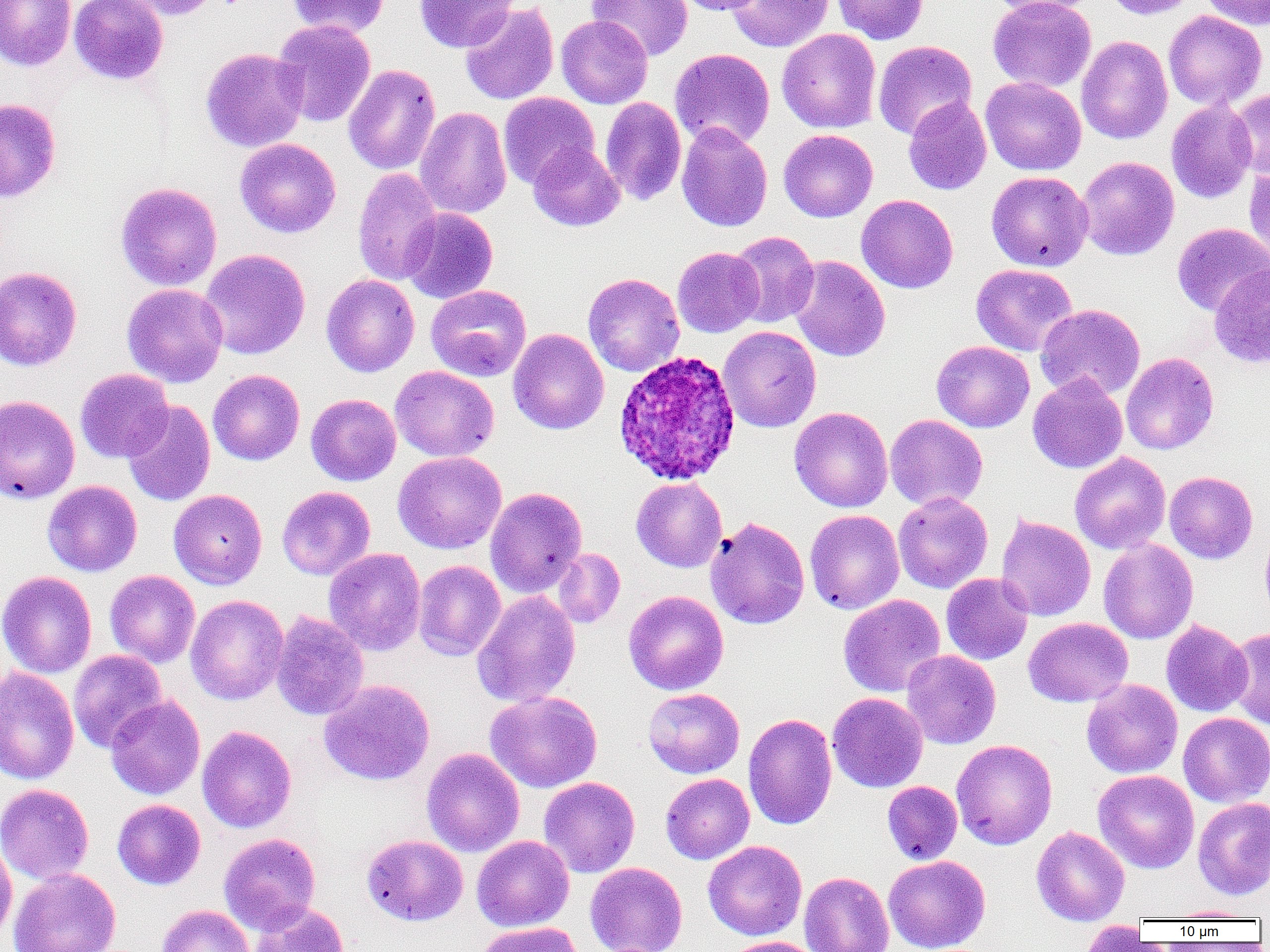

Approximate bounding boxes as named x1/y1/x2/y2 corners in pixels. Plasmodium ovale-infected red blood cell locations: (x1=613, y1=349, x2=741, y2=486). Uninfected red blood cell locations: (x1=0, y1=0, x2=76, y2=71), (x1=69, y1=0, x2=168, y2=85), (x1=116, y1=0, x2=223, y2=20), (x1=285, y1=0, x2=392, y2=38), (x1=415, y1=0, x2=518, y2=52), (x1=586, y1=0, x2=693, y2=61), (x1=674, y1=0, x2=765, y2=15), (x1=726, y1=0, x2=834, y2=52), (x1=832, y1=0, x2=929, y2=44), (x1=985, y1=0, x2=1098, y2=17), (x1=987, y1=0, x2=1096, y2=91), (x1=1102, y1=0, x2=1199, y2=19), (x1=1198, y1=0, x2=1270, y2=30), (x1=460, y1=3, x2=559, y2=105), (x1=1163, y1=10, x2=1267, y2=111), (x1=556, y1=15, x2=652, y2=108), (x1=273, y1=19, x2=376, y2=127), (x1=777, y1=28, x2=881, y2=133), (x1=1076, y1=35, x2=1173, y2=144), (x1=873, y1=40, x2=977, y2=140), (x1=200, y1=47, x2=308, y2=152), (x1=670, y1=48, x2=775, y2=150), (x1=343, y1=64, x2=440, y2=175), (x1=981, y1=77, x2=1086, y2=175), (x1=1228, y1=88, x2=1270, y2=179), (x1=498, y1=92, x2=599, y2=188), (x1=600, y1=97, x2=686, y2=206), (x1=903, y1=97, x2=992, y2=195), (x1=0, y1=98, x2=61, y2=202), (x1=1166, y1=100, x2=1257, y2=203), (x1=415, y1=106, x2=511, y2=219), (x1=676, y1=122, x2=772, y2=232), (x1=778, y1=129, x2=878, y2=222), (x1=235, y1=138, x2=341, y2=238), (x1=528, y1=143, x2=625, y2=231), (x1=1076, y1=156, x2=1180, y2=261), (x1=1243, y1=163, x2=1270, y2=267), (x1=352, y1=167, x2=443, y2=286), (x1=986, y1=171, x2=1093, y2=271), (x1=115, y1=182, x2=222, y2=291), (x1=856, y1=194, x2=958, y2=293), (x1=401, y1=207, x2=498, y2=304), (x1=1172, y1=223, x2=1269, y2=316), (x1=728, y1=231, x2=819, y2=328), (x1=672, y1=247, x2=764, y2=337), (x1=198, y1=249, x2=310, y2=360), (x1=789, y1=256, x2=890, y2=361), (x1=971, y1=264, x2=1077, y2=356), (x1=1209, y1=264, x2=1270, y2=369), (x1=0, y1=266, x2=82, y2=371), (x1=583, y1=273, x2=685, y2=377), (x1=321, y1=274, x2=419, y2=377), (x1=122, y1=283, x2=228, y2=387), (x1=426, y1=285, x2=531, y2=381), (x1=1035, y1=304, x2=1145, y2=401), (x1=718, y1=326, x2=821, y2=433), (x1=508, y1=328, x2=609, y2=434), (x1=931, y1=341, x2=1034, y2=432), (x1=1121, y1=352, x2=1218, y2=455), (x1=390, y1=365, x2=499, y2=462), (x1=75, y1=369, x2=173, y2=463), (x1=208, y1=369, x2=305, y2=465), (x1=1028, y1=373, x2=1127, y2=473), (x1=306, y1=393, x2=401, y2=486), (x1=0, y1=395, x2=80, y2=504), (x1=122, y1=401, x2=215, y2=506), (x1=789, y1=407, x2=893, y2=512), (x1=885, y1=414, x2=987, y2=511), (x1=393, y1=451, x2=506, y2=554), (x1=1069, y1=452, x2=1171, y2=554), (x1=1164, y1=471, x2=1258, y2=564), (x1=631, y1=477, x2=727, y2=572), (x1=43, y1=480, x2=142, y2=576), (x1=277, y1=486, x2=375, y2=580), (x1=485, y1=487, x2=587, y2=597), (x1=168, y1=489, x2=267, y2=589), (x1=893, y1=492, x2=993, y2=593), (x1=805, y1=509, x2=904, y2=614), (x1=995, y1=514, x2=1095, y2=622), (x1=705, y1=516, x2=810, y2=629), (x1=1260, y1=525, x2=1270, y2=623), (x1=1098, y1=539, x2=1198, y2=644), (x1=324, y1=548, x2=426, y2=655), (x1=553, y1=548, x2=625, y2=629), (x1=413, y1=560, x2=506, y2=661), (x1=105, y1=570, x2=200, y2=667), (x1=0, y1=571, x2=97, y2=678), (x1=941, y1=573, x2=1033, y2=664), (x1=472, y1=590, x2=581, y2=708), (x1=624, y1=590, x2=728, y2=695), (x1=186, y1=594, x2=288, y2=705), (x1=838, y1=594, x2=946, y2=697), (x1=272, y1=610, x2=369, y2=720), (x1=1023, y1=617, x2=1133, y2=707), (x1=1161, y1=619, x2=1253, y2=717), (x1=1226, y1=627, x2=1270, y2=729), (x1=68, y1=650, x2=167, y2=753), (x1=902, y1=650, x2=1001, y2=749), (x1=0, y1=667, x2=79, y2=785), (x1=319, y1=679, x2=435, y2=786), (x1=1082, y1=679, x2=1182, y2=778), (x1=643, y1=688, x2=745, y2=778), (x1=485, y1=690, x2=602, y2=792), (x1=828, y1=692, x2=928, y2=792), (x1=105, y1=696, x2=205, y2=800), (x1=743, y1=712, x2=837, y2=830), (x1=1178, y1=712, x2=1270, y2=806), (x1=197, y1=725, x2=296, y2=833), (x1=951, y1=739, x2=1057, y2=850), (x1=422, y1=747, x2=524, y2=857), (x1=1093, y1=770, x2=1199, y2=873), (x1=660, y1=773, x2=755, y2=864), (x1=539, y1=776, x2=640, y2=877), (x1=882, y1=781, x2=962, y2=864), (x1=0, y1=783, x2=94, y2=884), (x1=1193, y1=796, x2=1270, y2=900), (x1=112, y1=799, x2=205, y2=890), (x1=1031, y1=826, x2=1129, y2=925), (x1=219, y1=833, x2=320, y2=934), (x1=361, y1=834, x2=468, y2=926), (x1=472, y1=835, x2=574, y2=932), (x1=0, y1=838, x2=17, y2=945), (x1=703, y1=840, x2=807, y2=940), (x1=883, y1=855, x2=990, y2=952), (x1=585, y1=862, x2=688, y2=952), (x1=8, y1=867, x2=121, y2=952), (x1=799, y1=872, x2=894, y2=952), (x1=249, y1=902, x2=349, y2=952), (x1=156, y1=905, x2=254, y2=952), (x1=1169, y1=905, x2=1261, y2=921), (x1=1080, y1=921, x2=1148, y2=951), (x1=474, y1=922, x2=583, y2=952), (x1=722, y1=936, x2=823, y2=952). Slide-level diagnosis: Plasmodium ovale. 1000x magnification. Light microscopy. Thin blood smear. Image is 1270×952 pixels. Single field of view.